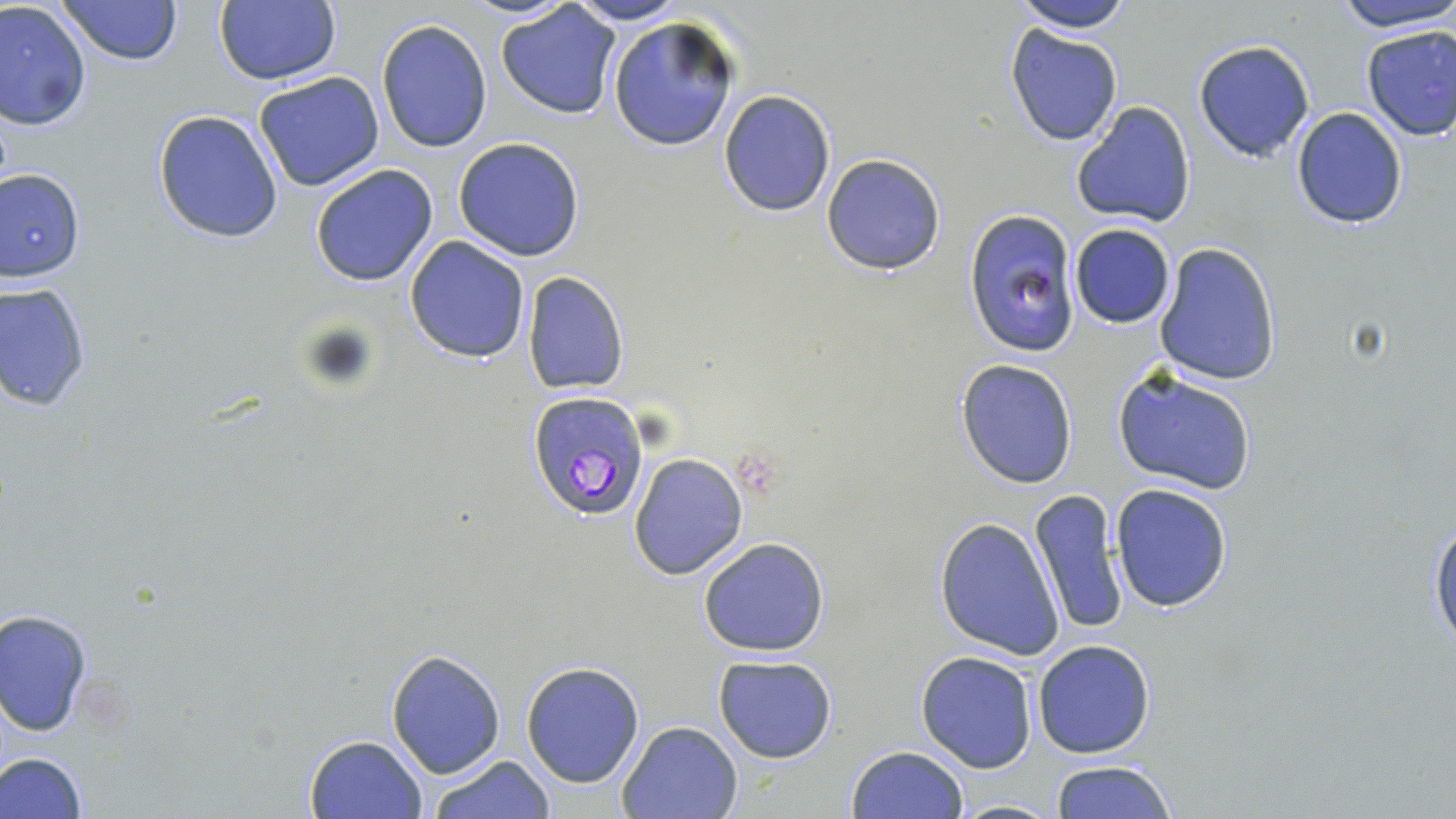

slide-level diagnosis = Plasmodium falciparum
field of view = one of a larger specimen
magnification = 1000x
stain = May-Grünwald-Giemsa
image size = 1456×819 pixels
Plasmodium falciparum-infected red blood cell locations = approximate bounding boxes as (x1,y1)-(x2,y2) corner pairs in pixels: (527,391)-(650,523)
uninfected red blood cell locations = approximate bounding boxes as (x1,y1)-(x2,y2) corner pairs in pixels: (57,0)-(184,67), (216,0)-(341,85), (567,0)-(689,25), (1009,0)-(1134,33), (1334,0)-(1454,33), (0,1)-(95,131), (496,3)-(622,119), (608,17)-(739,150), (375,19)-(492,154), (1004,24)-(1123,147), (1358,24)-(1456,141), (1193,39)-(1315,162), (255,71)-(385,192), (718,91)-(835,216), (1070,101)-(1198,229), (1291,106)-(1407,229), (153,109)-(285,243), (452,136)-(586,263), (821,153)-(946,274), (310,163)-(440,286), (0,169)-(85,282), (963,209)-(1081,353), (1068,223)-(1176,329), (404,236)-(531,363), (1154,242)-(1281,385), (523,272)-(628,394), (0,281)-(93,412), (955,358)-(1078,489), (1113,366)-(1259,496), (630,452)-(748,580), (1110,483)-(1232,611), (1028,489)-(1127,635), (1428,512)-(1456,652), (934,516)-(1066,661), (698,536)-(832,657), (1,607)-(93,735), (1032,639)-(1155,759), (384,649)-(506,777), (916,650)-(1038,773), (713,654)-(838,763), (521,661)-(646,788), (616,719)-(744,819), (303,733)-(429,819), (844,746)-(968,819), (1,751)-(89,819), (426,753)-(557,818), (1048,759)-(1179,819), (948,799)-(1065,817)
preparation = thin blood smear
modality = optical microscopy